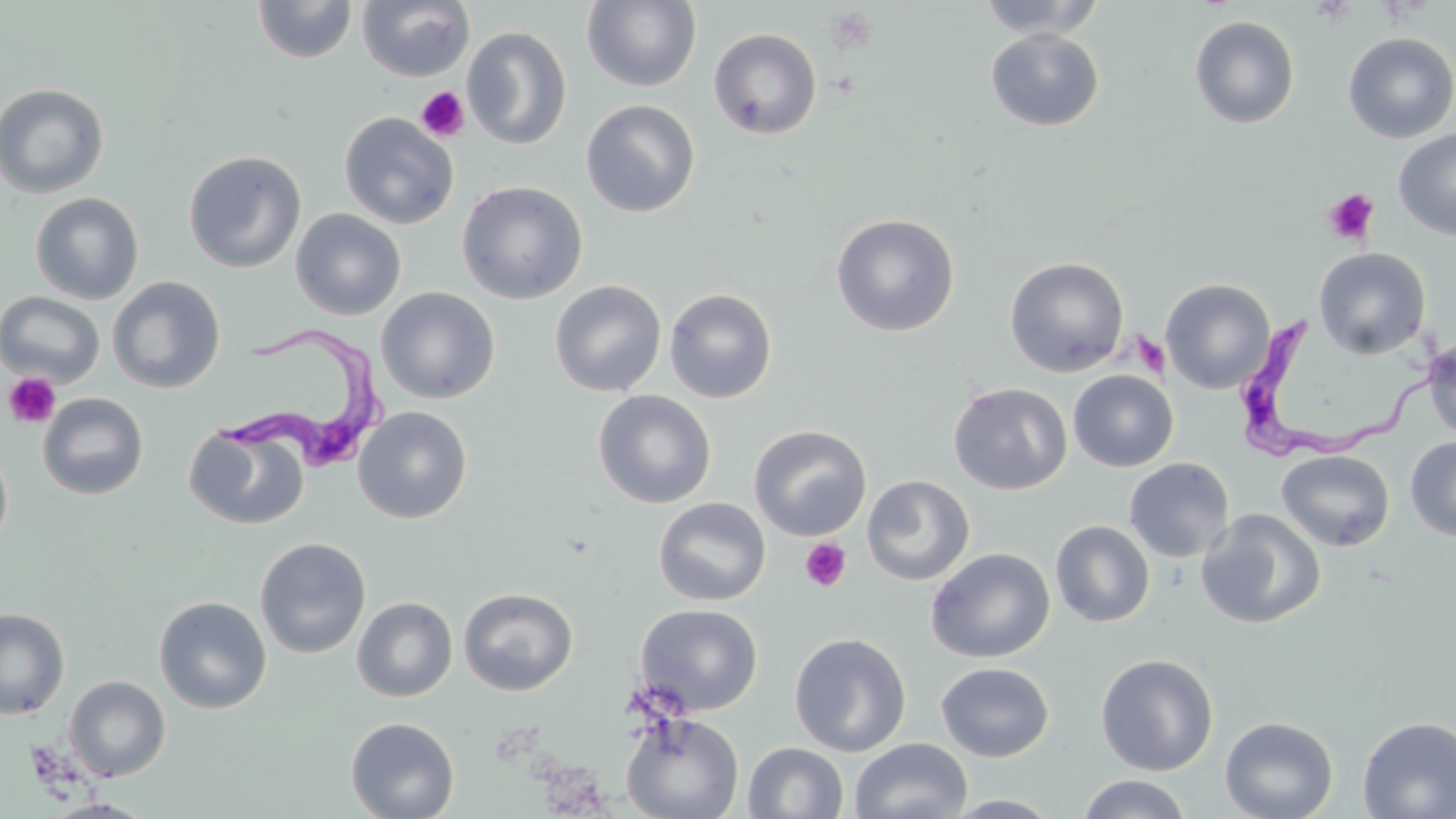
slide-level diagnosis = Trypanosoma brucei
preparation = thin blood film
stain = May-Grünwald-Giemsa
platelet locations = approximate bounding boxes as (x1, y1, x2, y2) in pixels: (416, 86, 469, 143), (1322, 188, 1380, 246), (1131, 332, 1170, 378), (3, 372, 62, 429), (799, 538, 852, 592)
image size = 1456×819 pixels
field of view = one of a larger specimen
Trypanosoma brucei locations = approximate bounding boxes as (x1, y1, x2, y2) in pixels: (1241, 310, 1452, 461), (213, 318, 395, 475)
uninfected red blood cell locations = approximate bounding boxes as (x1, y1, x2, y2) in pixels: (252, 0, 358, 64), (357, 0, 475, 83), (975, 0, 1106, 40), (582, 1, 702, 92), (1189, 16, 1300, 129), (462, 26, 572, 150), (709, 27, 822, 139), (985, 27, 1104, 131), (1342, 32, 1456, 142), (0, 82, 110, 199), (581, 99, 700, 217), (339, 111, 459, 230), (1394, 129, 1456, 240), (183, 150, 307, 273), (456, 180, 588, 304), (29, 192, 145, 304), (290, 208, 406, 320), (830, 213, 960, 337), (1314, 247, 1431, 360), (1004, 257, 1129, 377), (106, 276, 226, 393), (1161, 278, 1276, 394), (549, 279, 667, 397), (376, 286, 500, 404), (664, 287, 778, 404), (0, 291, 106, 388), (1422, 335, 1456, 443), (1067, 370, 1179, 472), (948, 381, 1072, 495), (593, 389, 716, 508), (38, 392, 148, 500), (353, 406, 472, 524), (184, 423, 309, 531), (749, 424, 871, 541), (1404, 436, 1456, 542), (0, 444, 14, 554), (1276, 450, 1394, 551), (1123, 457, 1234, 563), (862, 474, 975, 585), (653, 496, 771, 606), (1195, 509, 1326, 629), (1050, 520, 1155, 627), (254, 537, 371, 659), (925, 547, 1055, 663), (458, 587, 578, 697), (153, 596, 272, 714), (351, 596, 458, 702), (635, 603, 763, 715), (0, 607, 70, 719), (789, 632, 912, 757), (1096, 653, 1219, 775), (936, 662, 1054, 762), (64, 676, 170, 781), (621, 712, 745, 819), (1219, 715, 1339, 819), (1357, 716, 1456, 818), (345, 717, 460, 819), (850, 737, 973, 819), (743, 742, 849, 818), (1075, 773, 1193, 819), (943, 794, 1065, 818), (42, 797, 156, 818)
modality = light microscopy
magnification = 1000x